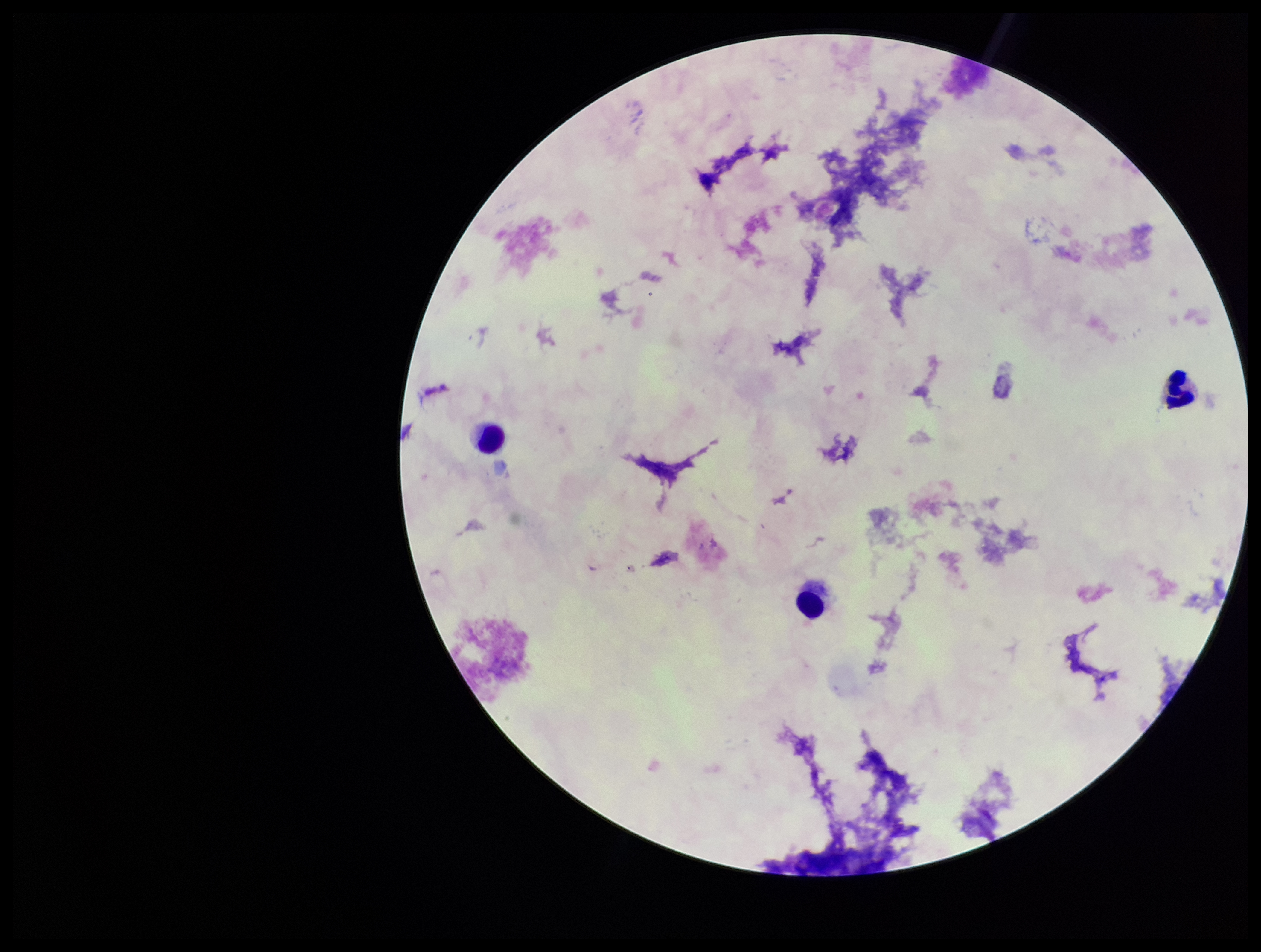
stain = Giemsa
leukocyte count = 3
patient malaria status = negative
image size = 1261×952 pixels
parasite count = 0
capture = smartphone photograph through the microscope eyepiece
preparation = thick
field of view = one from this slide
Plasmodium parasites = none seen